Outline each blood parasite and name the species.
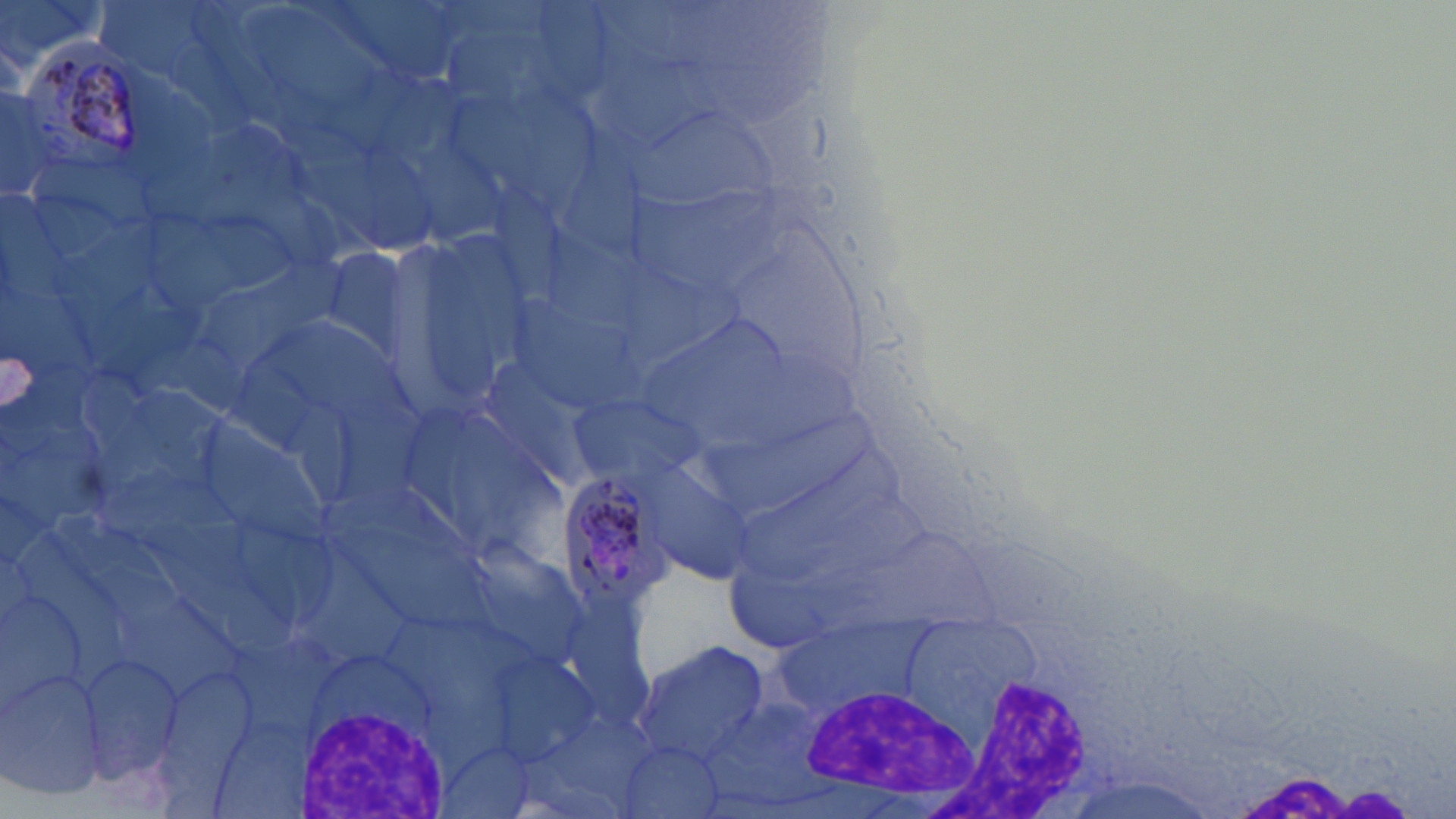
Approximate bounding boxes as [x1, y1, x2, y2] in pixels.
Plasmodium malariae-infected red blood cells: [25, 32, 142, 175], [555, 469, 678, 611].
No Plasmodium falciparum, Plasmodium ovale, Plasmodium vivax, Babesia divergens, or Trypanosoma brucei observed.

Summary:
  - White blood cell locations: [919, 666, 1089, 819], [795, 684, 976, 803], [299, 702, 447, 818]
  - Uninfected red blood cell locations: [382, 228, 546, 416], [313, 242, 420, 369], [569, 388, 702, 486], [637, 458, 761, 588], [628, 636, 770, 765], [79, 653, 184, 780], [2, 669, 111, 800]
  - Slide-level diagnosis: Plasmodium malariae
  - Modality: light microscopy
  - Preparation: thin blood film
  - Stain: May-Grünwald-Giemsa
  - Magnification: 1000x
  - Image size: 1456×819 pixels
  - Field of view: one of a larger specimen